Assess the morphology of the red blood cells.
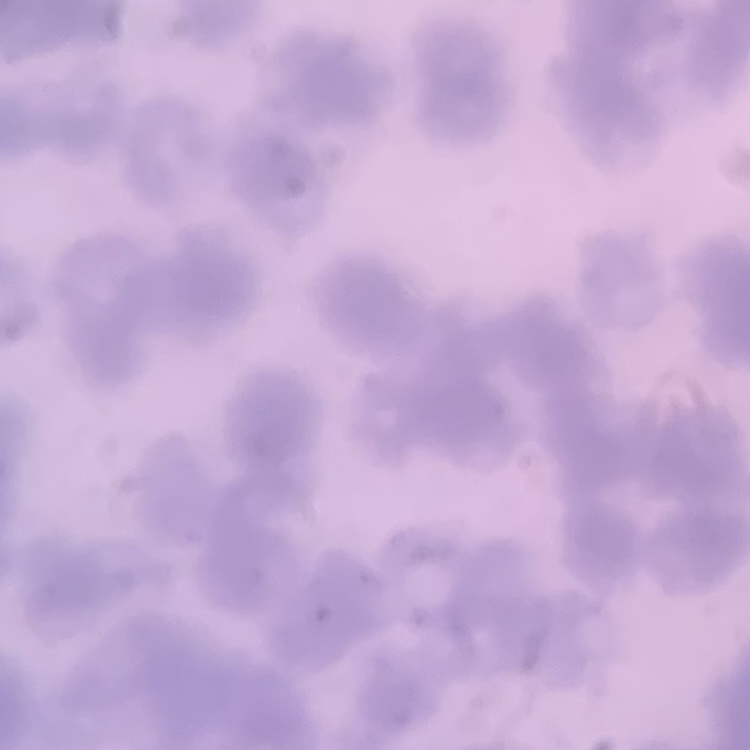
Rouleaux formation.

Summary:
  - Stain: Field's or Giemsa
  - Image type: square crop of a larger photomicrograph
  - Preparation: thin blood smear